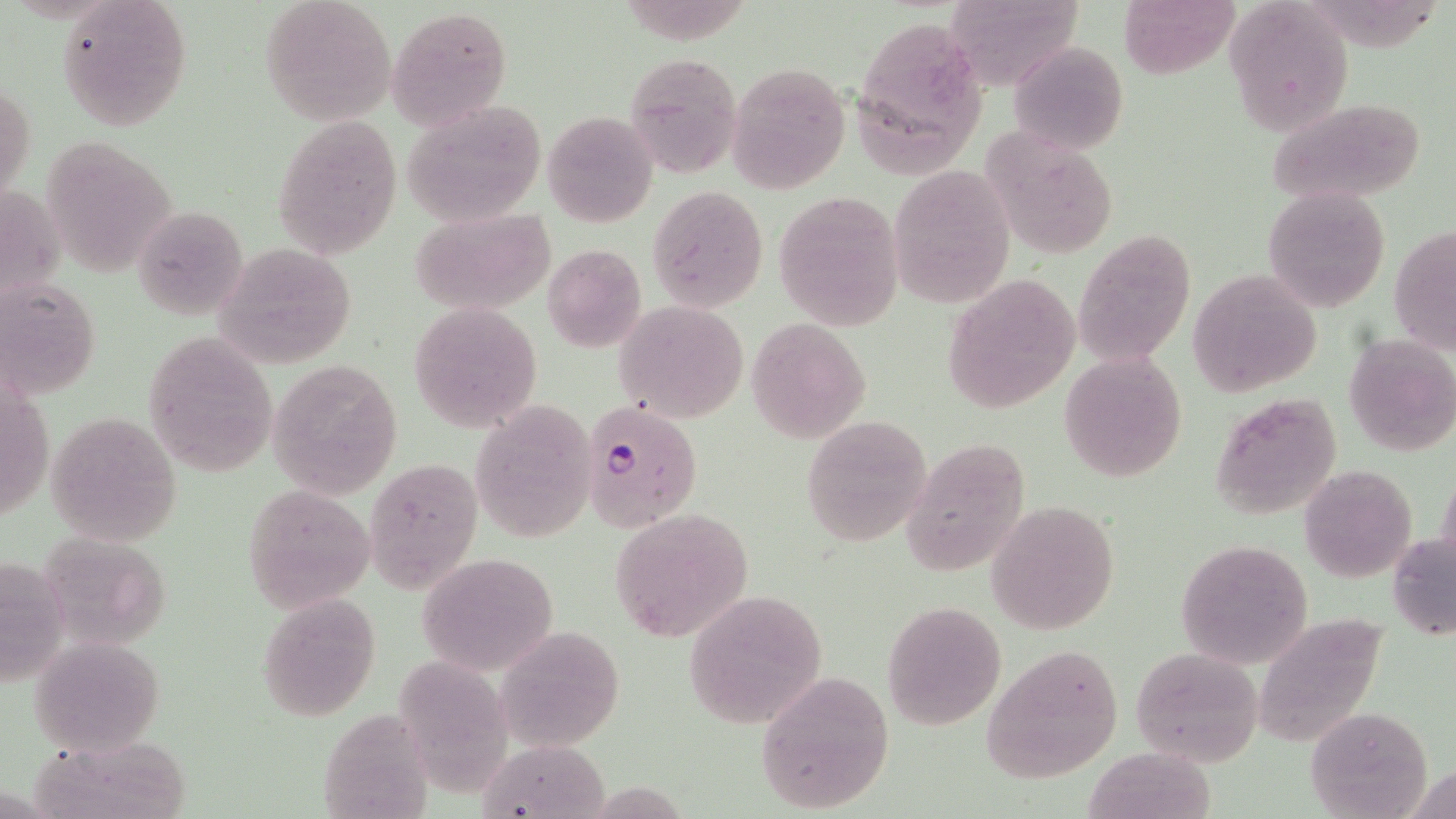

Summary:
  - Coordinate format: approximate bounding boxes as (x1, y1, x2, y2) in pixels
  - Plasmodium falciparum-infected red blood cell locations: (583, 403, 703, 531)
  - Uninfected red blood cell locations: (56, 0, 195, 130), (260, 0, 396, 124), (1118, 0, 1237, 76), (948, 2, 1090, 94), (1227, 4, 1353, 135), (387, 6, 513, 128), (854, 11, 988, 172), (1007, 41, 1129, 154), (623, 53, 742, 179), (727, 62, 850, 193), (1, 80, 36, 209), (1268, 97, 1429, 204), (402, 98, 549, 226), (542, 109, 658, 227), (271, 113, 403, 258), (984, 131, 1120, 260), (51, 145, 182, 283), (890, 166, 1015, 308), (3, 177, 64, 298), (647, 186, 769, 312), (1263, 186, 1391, 313), (774, 194, 905, 330), (132, 205, 250, 321), (409, 208, 557, 314), (1390, 226, 1456, 356), (1074, 230, 1196, 365), (213, 244, 356, 367), (542, 244, 647, 352), (1188, 269, 1322, 397), (941, 275, 1078, 411), (2, 280, 102, 402), (408, 300, 543, 433), (614, 301, 749, 423), (747, 320, 871, 443), (142, 329, 279, 475), (1343, 335, 1456, 458), (1058, 353, 1188, 481), (269, 358, 402, 500), (0, 375, 60, 523), (1210, 390, 1343, 522), (469, 401, 597, 542), (47, 411, 182, 545), (801, 417, 932, 545), (901, 436, 1031, 574), (364, 460, 480, 591), (1299, 465, 1417, 584), (1436, 467, 1455, 576), (243, 483, 376, 613), (987, 502, 1119, 634), (610, 506, 755, 644), (1389, 533, 1456, 640), (1176, 537, 1314, 669), (415, 551, 560, 677), (0, 555, 71, 685), (686, 591, 828, 728), (254, 592, 382, 720), (881, 601, 1005, 730), (1271, 614, 1390, 744), (504, 633, 621, 752), (31, 638, 165, 753), (401, 641, 511, 798), (982, 646, 1124, 781), (1129, 648, 1262, 766), (755, 672, 895, 815), (315, 701, 440, 819), (1305, 705, 1434, 818), (29, 732, 200, 818), (483, 740, 610, 819), (1086, 747, 1223, 816)
  - Slide-level diagnosis: Plasmodium falciparum
  - Stain: May-Grünwald-Giemsa
  - Field of view: single
  - Image size: 1456×819 pixels
  - Preparation: thin blood film
  - Magnification: 1000x
  - Modality: light microscopy